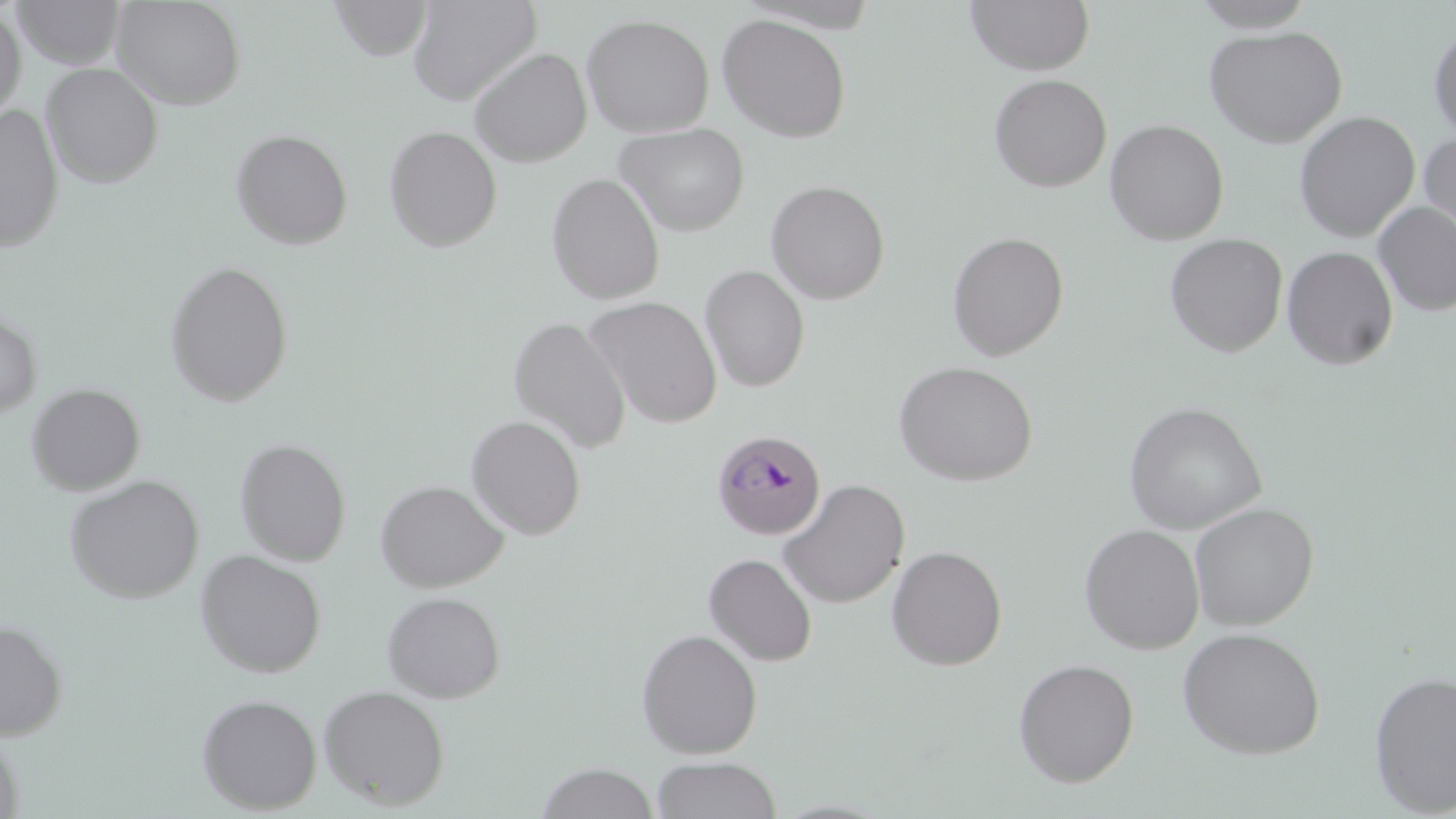

Summary:
  - Coordinate format: approximate bounding boxes as [x1, y1, x2, y2] in pixels
  - Uninfected red blood cell locations: [13, 0, 125, 70], [112, 0, 247, 110], [329, 0, 433, 61], [407, 0, 542, 107], [965, 0, 1095, 76], [1189, 0, 1319, 32], [0, 5, 26, 122], [581, 13, 715, 138], [717, 14, 852, 143], [1428, 24, 1456, 140], [1203, 25, 1348, 148], [468, 47, 592, 167], [42, 62, 164, 188], [988, 74, 1112, 192], [0, 103, 63, 253], [1294, 111, 1420, 242], [1104, 119, 1229, 246], [614, 123, 750, 237], [384, 125, 502, 252], [230, 128, 353, 250], [1418, 133, 1456, 252], [546, 173, 665, 305], [766, 180, 890, 304], [1373, 202, 1456, 317], [946, 231, 1069, 361], [1164, 233, 1288, 357], [1282, 246, 1399, 369], [164, 259, 293, 407], [699, 265, 810, 392], [583, 295, 723, 428], [0, 309, 42, 420], [508, 316, 632, 455], [893, 360, 1039, 486], [27, 382, 145, 495], [1124, 401, 1266, 534], [465, 415, 586, 540], [235, 437, 351, 566], [66, 475, 204, 603], [375, 479, 508, 592], [777, 479, 910, 609], [1189, 502, 1319, 631], [1079, 523, 1205, 655], [886, 545, 1007, 671], [195, 549, 326, 678], [703, 553, 817, 666], [381, 590, 506, 703], [0, 620, 68, 740], [1177, 627, 1326, 759], [636, 628, 762, 759], [1012, 658, 1139, 787], [1369, 669, 1456, 816], [318, 684, 451, 810], [196, 693, 322, 814], [0, 731, 25, 819], [650, 756, 782, 818], [535, 762, 658, 819]
  - Plasmodium malariae-infected red blood cell locations: [711, 429, 827, 540]
  - Slide-level diagnosis: Plasmodium malariae
  - Stain: May-Grünwald-Giemsa
  - Modality: light microscopy
  - Preparation: thin blood film
  - Image size: 1456×819 pixels
  - Magnification: 1000x
  - Field of view: one of a larger specimen